Assess this cell for malaria.
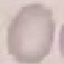

It is uninfected.

preparation = thin blood film
image type = automatically extracted cell patch, resized to 64 × 64 pixels
capture = smartphone through the microscope eyepiece
stain = Giemsa